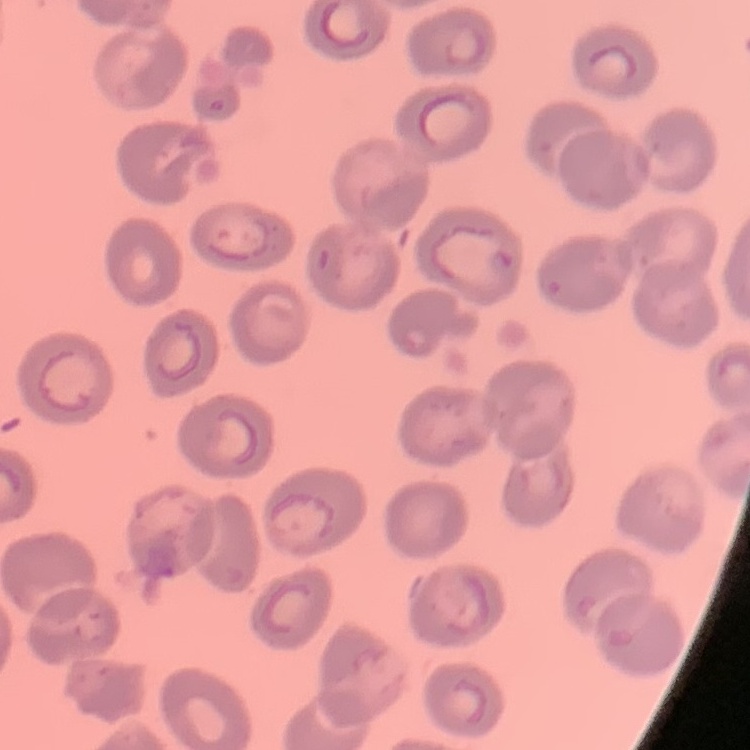

The red blood cells exhibit no rouleaux formation. Thin blood smear. Stained with either Field's or Giemsa. One tile cut from a larger photomicrograph.